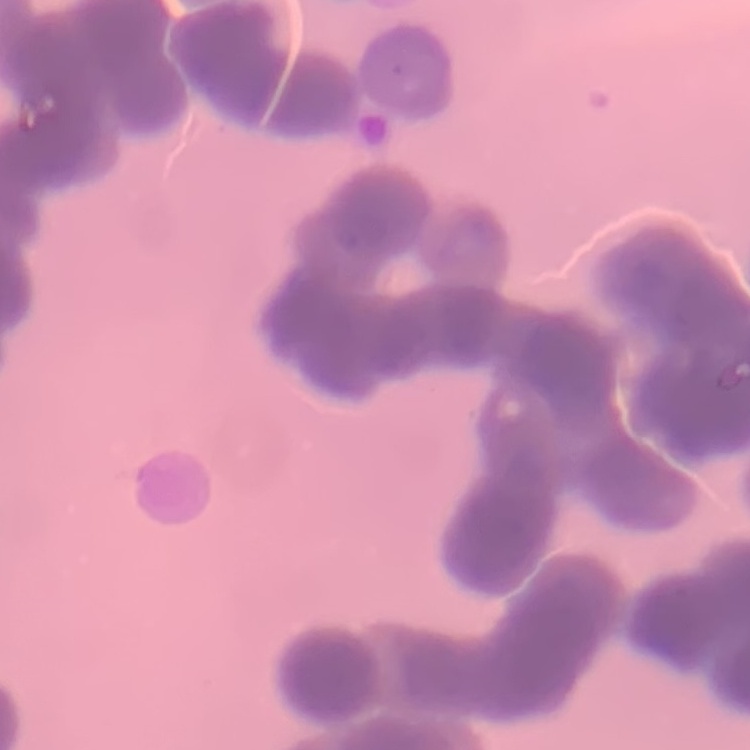

Summary:
  - Red blood cell morphology: rouleaux formation
  - Stain: Field's or Giemsa
  - Preparation: thin blood smear
  - Image type: one tile cut from a larger photomicrograph